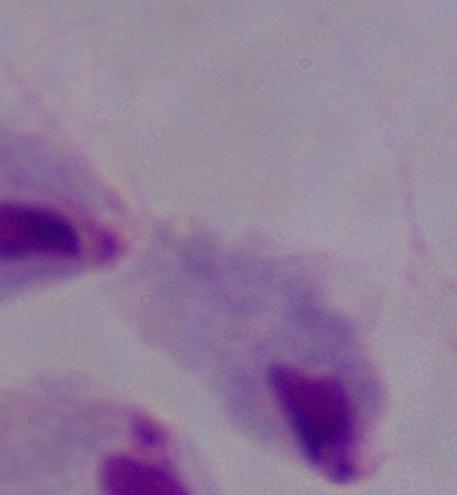

1000x magnification. A trichomonad is seen. Micrograph.